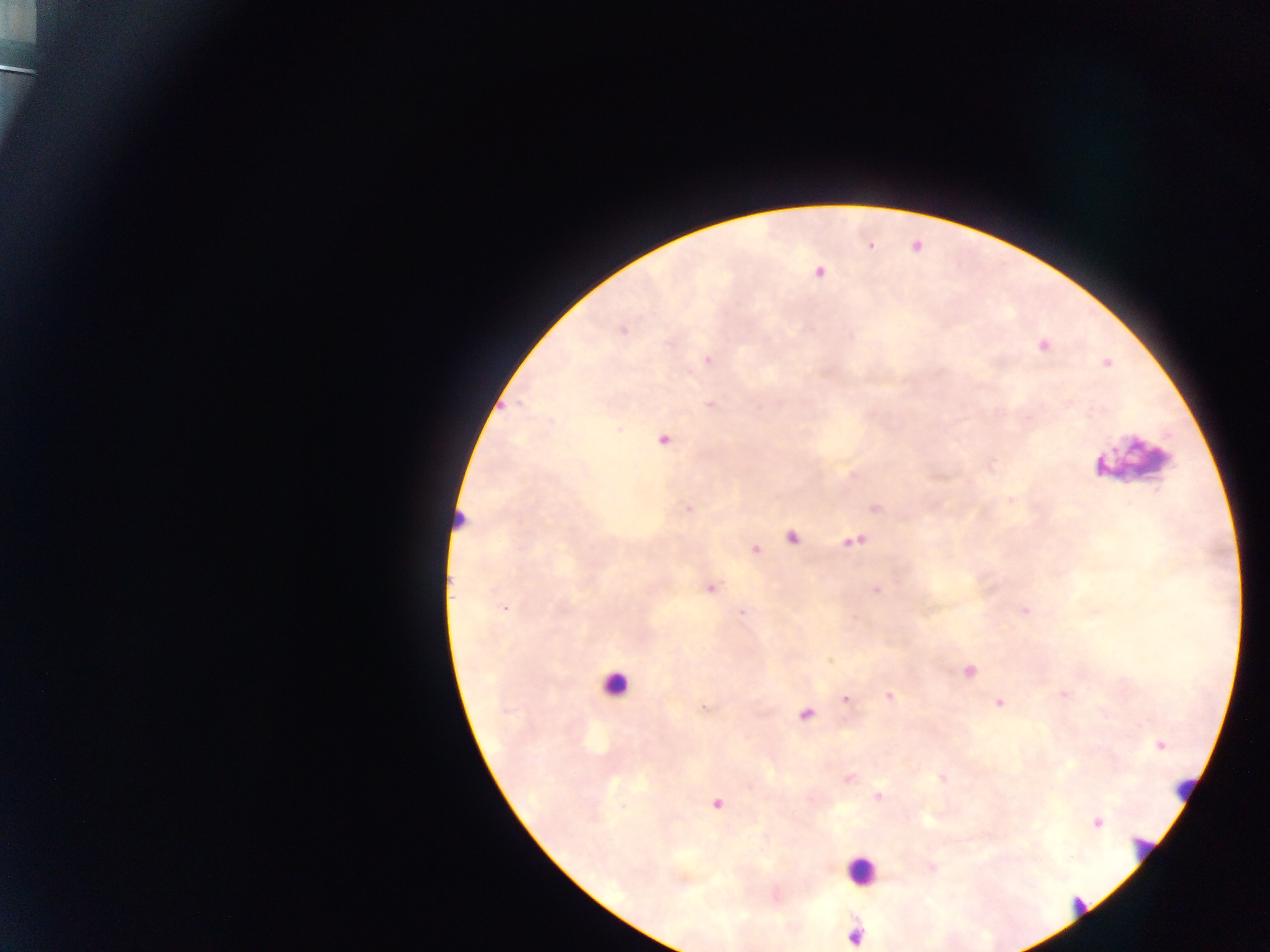
Approximate centers as {x, y} in pixels. Leukocyte locations (subset; some below the resolvable size): {1134, 459}, {461, 516}, {615, 684}, {1182, 788}, {1143, 847}, {861, 870}, {1077, 908}, {852, 935}. Plasmodium parasite locations: {870, 246}, {820, 273}, {623, 331}, {1044, 345}, {707, 359}, {1107, 363}, {711, 405}, {663, 440}, {688, 508}, {876, 508}, {792, 538}, {854, 541}, {755, 549}, {711, 588}, {877, 590}, {505, 608}, {1025, 610}, {742, 611}, {854, 618}, {969, 671}, {1065, 693}, {890, 696}, {845, 699}, {999, 702}, {703, 707}, {805, 714}, {1160, 746}, {848, 778}, {942, 778}, {878, 795}, {717, 803}, {1098, 823}. Collected in Ghana. Thick blood smear. Image is 1270×952 pixels. One field of view. Mobile-phone photograph taken through the microscope.